Mark where platelets are.
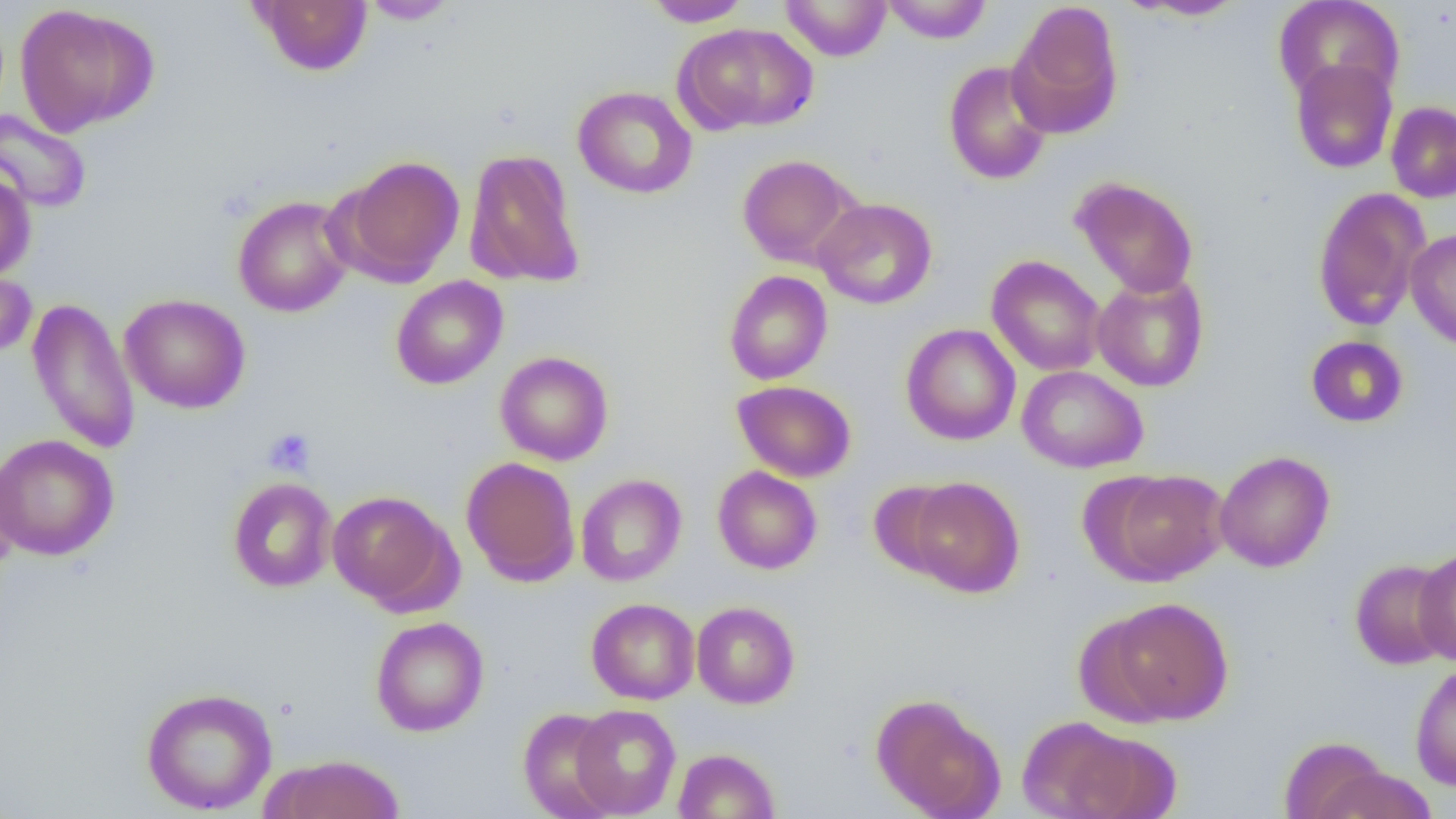
Approximate bounding boxes as (x1, y1, x2, y2) in pixels.
Platelets: (263, 428, 316, 477).

Uninfected red blood cell locations: (249, 0, 373, 76), (642, 0, 753, 27), (780, 0, 892, 61), (881, 0, 993, 44), (1273, 0, 1404, 106), (360, 1, 460, 24), (1126, 1, 1249, 21), (1009, 2, 1124, 138), (15, 4, 157, 136), (676, 22, 818, 134), (1289, 57, 1398, 174), (942, 60, 1053, 185), (573, 86, 697, 199), (1386, 101, 1456, 203), (0, 109, 92, 214), (464, 148, 585, 290), (737, 154, 859, 268), (337, 155, 466, 285), (0, 168, 36, 281), (1070, 176, 1199, 298), (1312, 187, 1430, 331), (232, 195, 354, 318), (813, 198, 937, 309), (1405, 228, 1456, 350), (986, 255, 1106, 377), (0, 266, 36, 362), (724, 270, 833, 385), (1091, 271, 1209, 392), (391, 275, 508, 390), (119, 293, 251, 414), (26, 296, 140, 456), (901, 323, 1021, 445), (1306, 335, 1409, 428), (495, 351, 614, 465), (1017, 365, 1148, 473), (732, 380, 857, 482), (0, 434, 118, 561), (1214, 451, 1335, 572), (0, 454, 22, 576), (461, 457, 580, 587), (712, 466, 823, 574), (1100, 470, 1230, 585), (575, 473, 687, 586), (906, 476, 1025, 598), (228, 477, 337, 593), (868, 480, 963, 578), (327, 490, 455, 609), (1415, 546, 1456, 666), (1349, 559, 1453, 669), (1103, 597, 1232, 725), (586, 598, 700, 705), (691, 601, 800, 709), (371, 616, 489, 736), (1410, 662, 1456, 790), (140, 687, 278, 814), (871, 693, 1004, 819), (571, 704, 681, 817), (518, 708, 622, 819), (1017, 715, 1144, 819), (1070, 729, 1182, 819), (1279, 736, 1391, 819), (673, 748, 780, 818), (261, 754, 406, 819), (1315, 766, 1437, 819). Slide-level diagnosis: negative for blood parasites. Image is 1456×819 pixels. Thin blood smear. One field of a larger specimen. 1000x magnification. Optical microscopy.